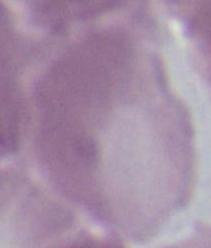

1000x magnification. Photomicrograph. A red blood cell is seen.